Identify the preparation type.
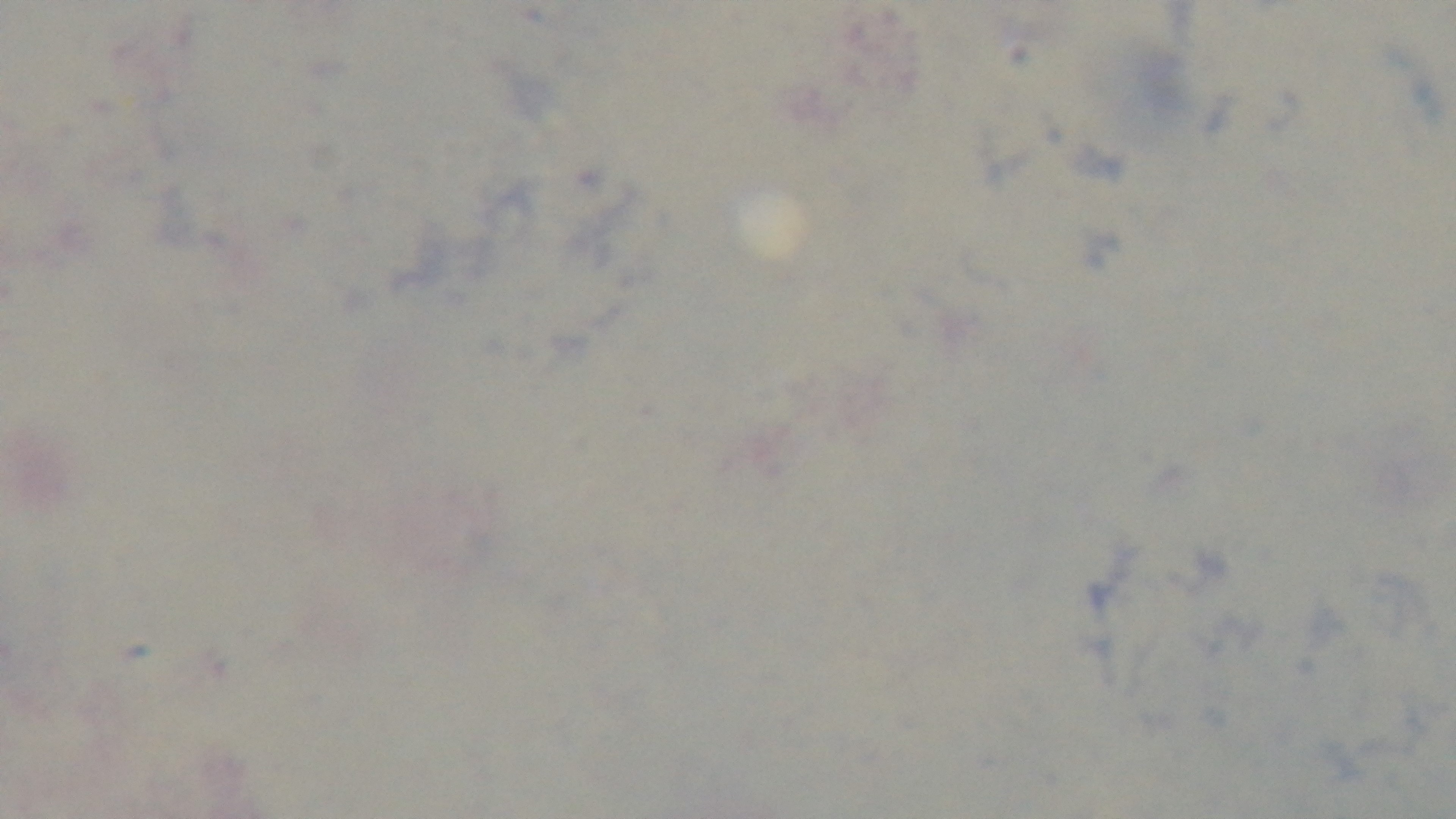

It is a thick blood film.

Summary:
  - Capture: mounted 4K digital camera
  - Stain: Giemsa
  - Modality: light microscopy
  - Field of view: single
  - Malaria status: negative
  - Objective: 100x oil immersion